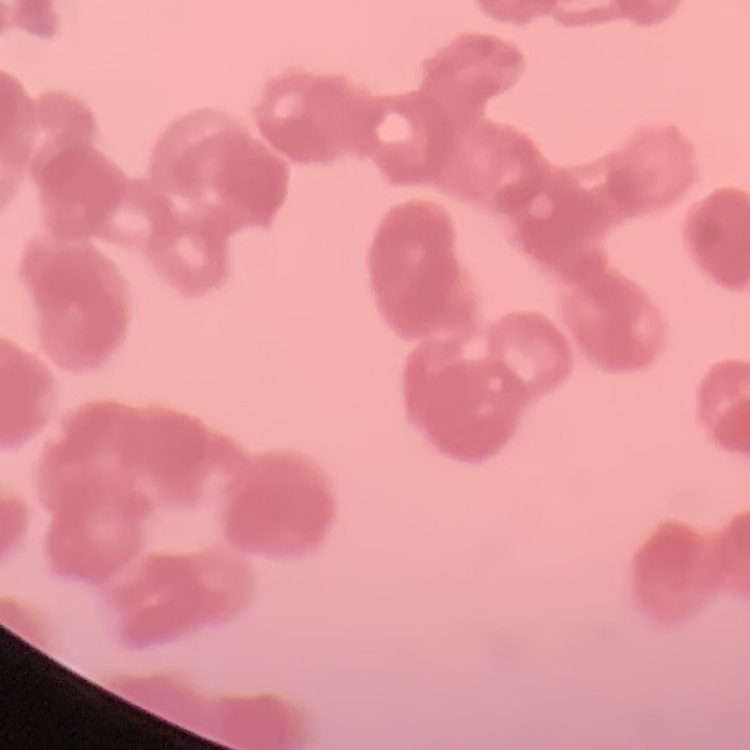

erythrocyte_morphology: rouleaux formation
image_type: square crop of a larger photomicrograph
stain: Field's or Giemsa
preparation: thin blood smear